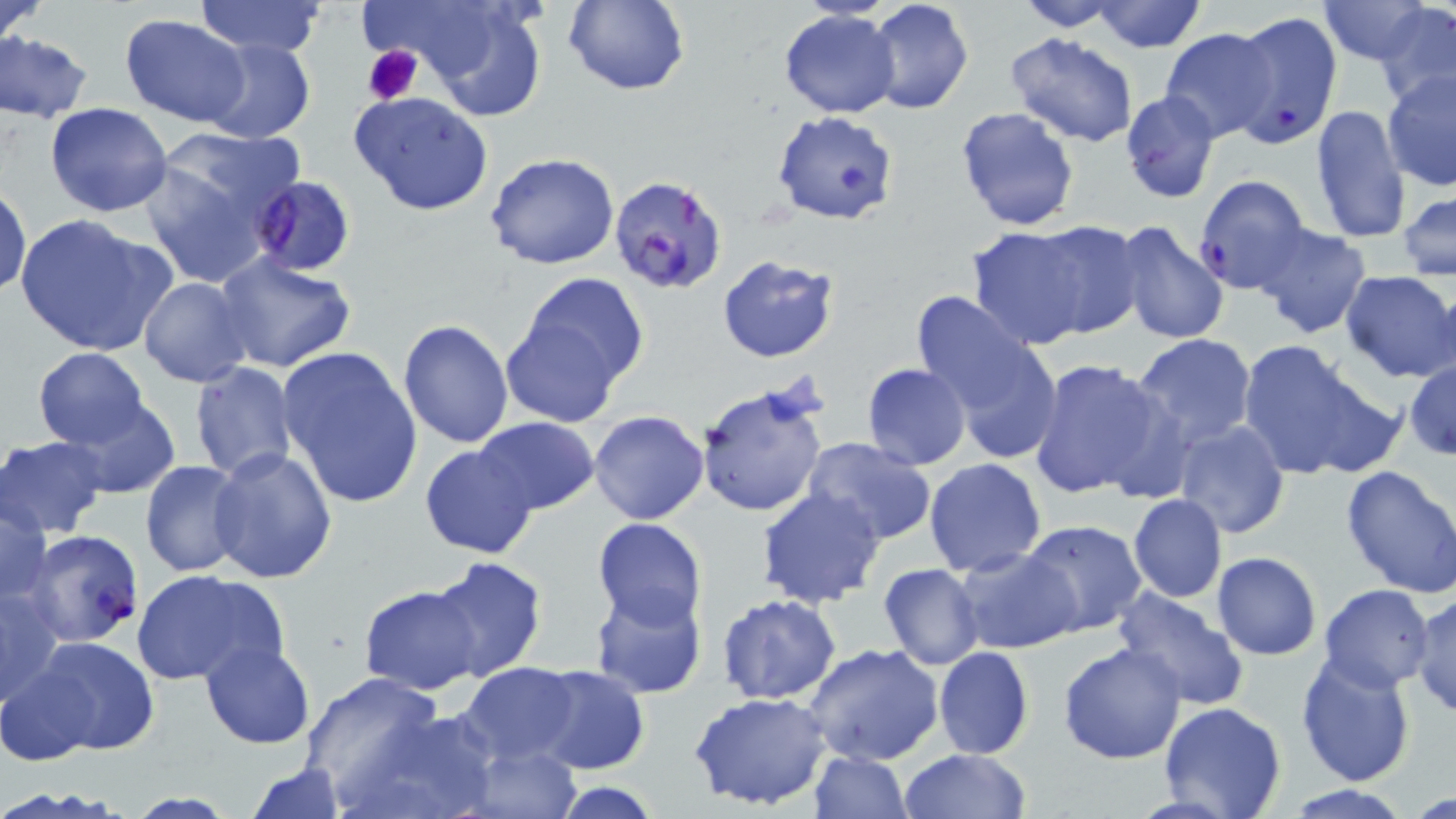 Approximate bounding boxes as named x1/y1/x2/y2 corners in pixels. Plasmodium falciparum-infected red blood cell locations: (x1=1228, y1=11, x2=1343, y2=148), (x1=250, y1=173, x2=359, y2=276), (x1=608, y1=174, x2=728, y2=295), (x1=1192, y1=176, x2=1311, y2=295), (x1=17, y1=529, x2=147, y2=649). Uninfected red blood cell locations: (x1=0, y1=0, x2=49, y2=48), (x1=193, y1=0, x2=327, y2=57), (x1=388, y1=0, x2=548, y2=121), (x1=561, y1=0, x2=690, y2=95), (x1=866, y1=0, x2=976, y2=114), (x1=1009, y1=0, x2=1127, y2=32), (x1=1088, y1=0, x2=1208, y2=53), (x1=1319, y1=0, x2=1438, y2=64), (x1=1375, y1=3, x2=1456, y2=108), (x1=779, y1=10, x2=900, y2=119), (x1=121, y1=15, x2=251, y2=127), (x1=1160, y1=27, x2=1279, y2=142), (x1=1, y1=32, x2=95, y2=123), (x1=1008, y1=33, x2=1138, y2=146), (x1=199, y1=36, x2=316, y2=146), (x1=1132, y1=43, x2=1260, y2=188), (x1=972, y1=45, x2=1117, y2=193), (x1=1381, y1=67, x2=1456, y2=191), (x1=350, y1=91, x2=494, y2=215), (x1=1120, y1=91, x2=1222, y2=204), (x1=45, y1=103, x2=173, y2=217), (x1=1310, y1=104, x2=1411, y2=245), (x1=954, y1=106, x2=1080, y2=232), (x1=770, y1=109, x2=899, y2=225), (x1=140, y1=129, x2=300, y2=289), (x1=486, y1=153, x2=620, y2=271), (x1=1, y1=182, x2=31, y2=299), (x1=1398, y1=190, x2=1456, y2=281), (x1=14, y1=213, x2=177, y2=358), (x1=1027, y1=220, x2=1145, y2=341), (x1=1113, y1=222, x2=1231, y2=348), (x1=1253, y1=223, x2=1371, y2=339), (x1=966, y1=225, x2=1097, y2=349), (x1=212, y1=252, x2=358, y2=374), (x1=716, y1=254, x2=840, y2=364), (x1=517, y1=271, x2=649, y2=397), (x1=1339, y1=271, x2=1456, y2=382), (x1=138, y1=278, x2=253, y2=387), (x1=915, y1=295, x2=1058, y2=457), (x1=500, y1=311, x2=624, y2=426), (x1=398, y1=318, x2=515, y2=448), (x1=1130, y1=334, x2=1257, y2=453), (x1=1238, y1=338, x2=1398, y2=482), (x1=927, y1=345, x2=1059, y2=558), (x1=276, y1=347, x2=423, y2=510), (x1=33, y1=348, x2=150, y2=447), (x1=1144, y1=353, x2=1276, y2=529), (x1=1027, y1=359, x2=1175, y2=502), (x1=1405, y1=359, x2=1456, y2=460), (x1=189, y1=362, x2=299, y2=481), (x1=862, y1=363, x2=971, y2=470), (x1=696, y1=385, x2=829, y2=518), (x1=61, y1=397, x2=180, y2=498), (x1=588, y1=411, x2=710, y2=526), (x1=474, y1=418, x2=599, y2=515), (x1=1172, y1=419, x2=1289, y2=538), (x1=0, y1=434, x2=110, y2=538), (x1=802, y1=438, x2=938, y2=547), (x1=420, y1=443, x2=540, y2=560), (x1=209, y1=445, x2=340, y2=582), (x1=923, y1=457, x2=1046, y2=577), (x1=139, y1=459, x2=250, y2=579), (x1=1339, y1=463, x2=1456, y2=599), (x1=757, y1=486, x2=886, y2=608), (x1=1, y1=491, x2=53, y2=605), (x1=1128, y1=494, x2=1227, y2=602), (x1=592, y1=518, x2=708, y2=632), (x1=1019, y1=520, x2=1148, y2=637), (x1=954, y1=546, x2=1081, y2=653), (x1=1212, y1=552, x2=1322, y2=660), (x1=426, y1=557, x2=548, y2=683), (x1=879, y1=562, x2=984, y2=670), (x1=132, y1=568, x2=285, y2=687), (x1=2, y1=580, x2=65, y2=710), (x1=1112, y1=583, x2=1247, y2=713), (x1=1319, y1=583, x2=1435, y2=691), (x1=358, y1=585, x2=484, y2=694), (x1=589, y1=585, x2=707, y2=701), (x1=1408, y1=590, x2=1456, y2=717), (x1=716, y1=595, x2=842, y2=706), (x1=29, y1=636, x2=161, y2=758), (x1=199, y1=641, x2=316, y2=749), (x1=1057, y1=642, x2=1186, y2=765), (x1=803, y1=643, x2=947, y2=767), (x1=933, y1=646, x2=1034, y2=759), (x1=1295, y1=651, x2=1416, y2=790), (x1=2, y1=658, x2=102, y2=766), (x1=458, y1=662, x2=581, y2=766), (x1=528, y1=664, x2=650, y2=775), (x1=297, y1=669, x2=452, y2=810), (x1=689, y1=692, x2=835, y2=812), (x1=1158, y1=702, x2=1286, y2=818), (x1=354, y1=706, x2=503, y2=819), (x1=463, y1=743, x2=582, y2=819), (x1=899, y1=748, x2=1032, y2=819), (x1=809, y1=750, x2=911, y2=819), (x1=246, y1=760, x2=346, y2=819), (x1=552, y1=780, x2=665, y2=819), (x1=1278, y1=783, x2=1417, y2=817). Platelet locations: (x1=363, y1=46, x2=423, y2=106). Slide-level diagnosis: Plasmodium falciparum. May-Grünwald-Giemsa-stained preparation. Captured at 1000x magnification. Optical microscopy. Image is 1456×819 pixels. Thin blood film. Single field of view.